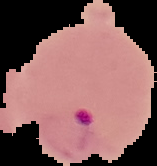
image_type: segmented cell region on a black background
image_size: 157×166 pixels
preparation: thin blood smear
result: Plasmodium parasites identified